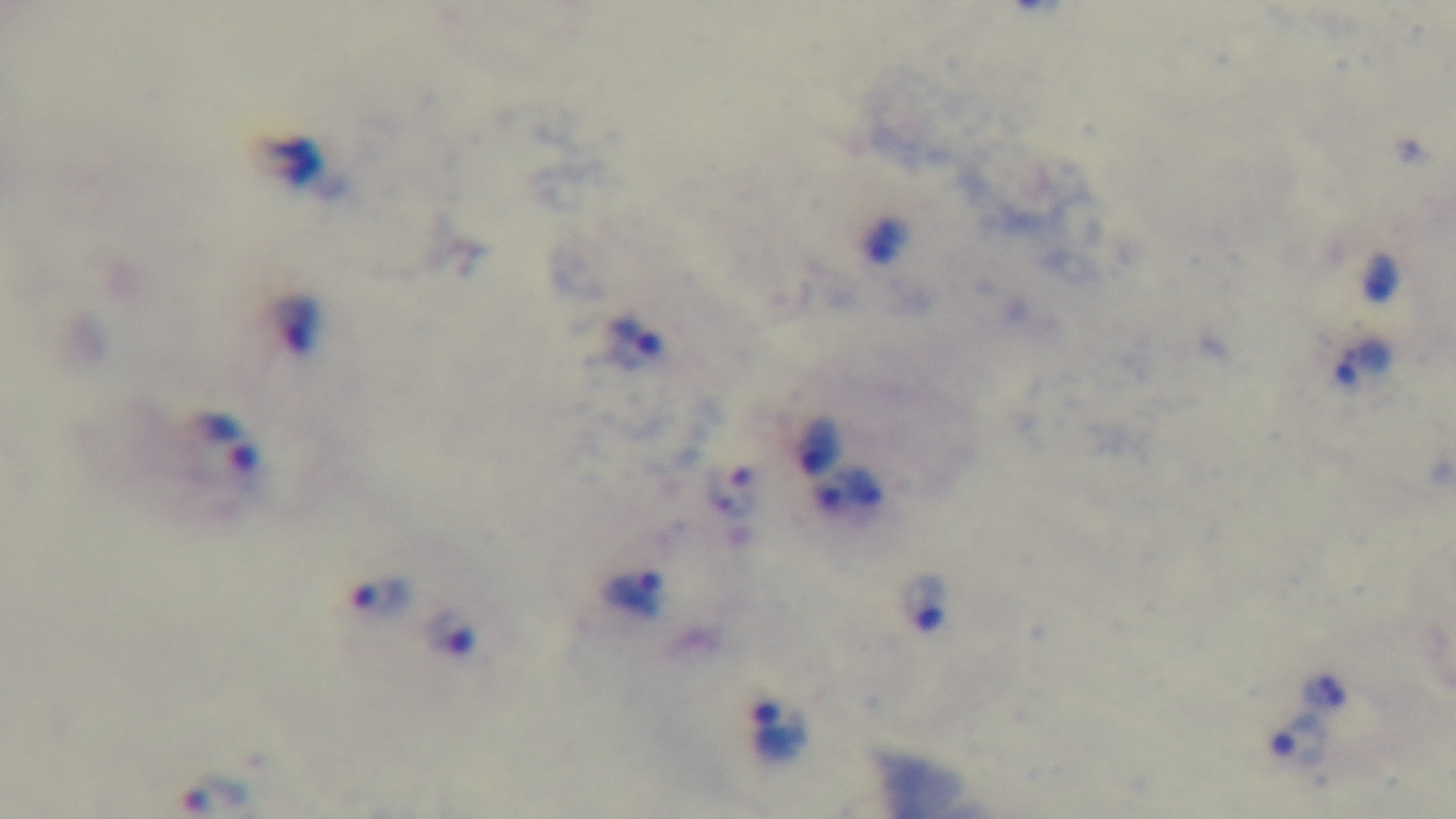

Summary:
  - Field of view: single
  - Modality: light microscopy
  - Preparation: thick smear
  - Stain: Giemsa
  - Objective: 100x oil immersion
  - Capture: mounted 4K digital camera
  - Malaria status: positive